Locate the red blood cells and classify each one as P. falciparum-infected, uninfected, or of indeterminate infection status.
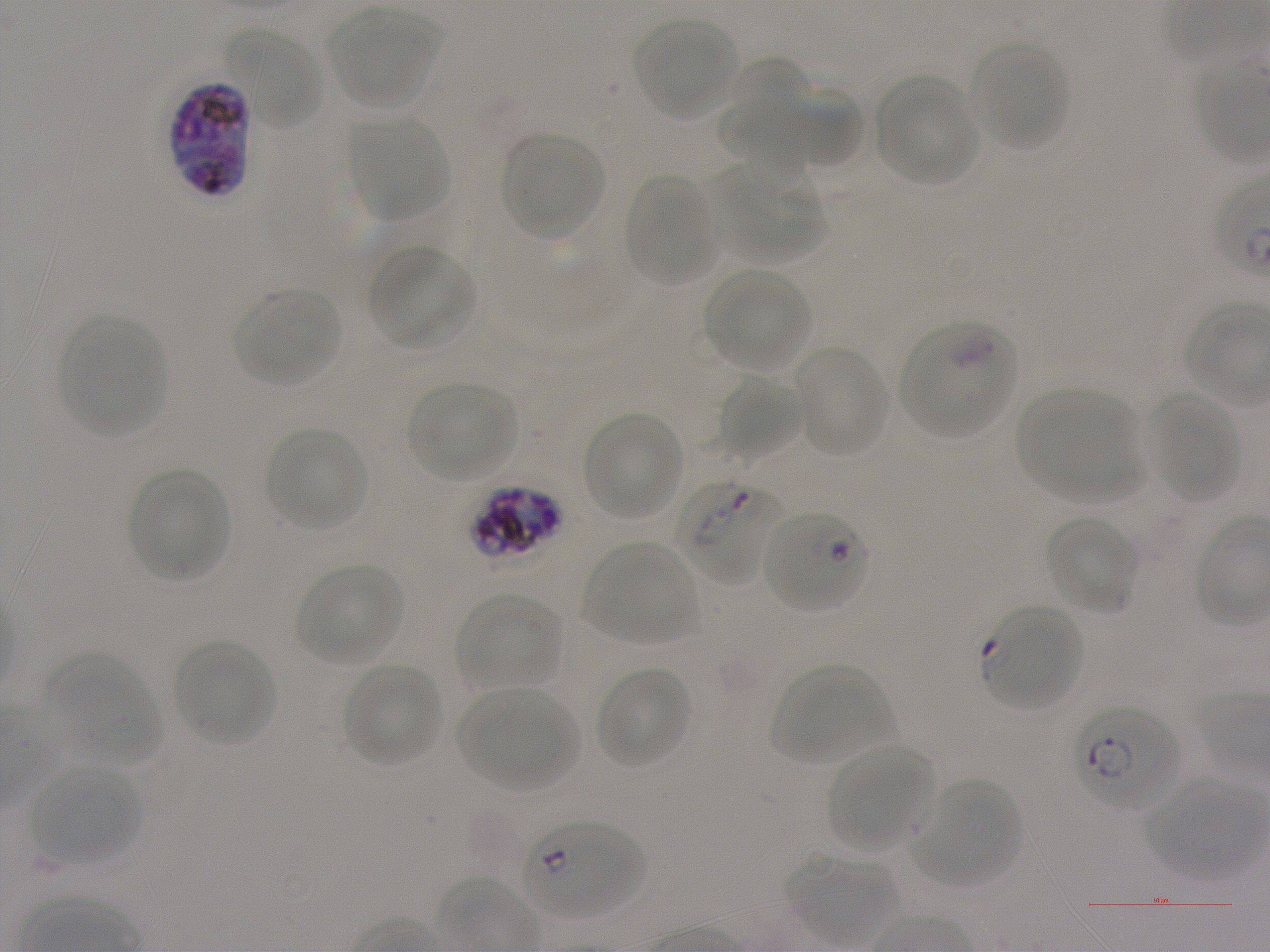

Approximate bounding boxes as (x1, y1, x2, y2) in pixels. Not every red blood cell is marked. A life-cycle stage — or a range of stages, where the recorded stages span more than one — follows each staged infected red blood cell.
Infected red blood cells: (169, 80, 252, 198); (674, 479, 785, 585) early ring to early trophozoite; (470, 484, 564, 561) schizont; (762, 508, 871, 613) early ring; (980, 604, 1083, 712) ring; (1072, 704, 1183, 812) early ring to early trophozoite; (522, 819, 647, 920) ring.
Red blood cells of indeterminate infection status: (898, 322, 1016, 437).
Uninfected red blood cells: (328, 9, 443, 111), (634, 18, 738, 120), (227, 25, 326, 130), (970, 42, 1070, 151), (725, 56, 812, 193), (873, 74, 979, 186), (783, 84, 864, 170), (716, 98, 813, 161), (347, 115, 450, 222), (502, 133, 605, 240), (712, 164, 824, 263), (624, 175, 718, 285), (367, 245, 477, 352), (703, 268, 812, 371), (234, 289, 341, 388), (60, 315, 167, 437), (792, 344, 890, 458), (716, 374, 803, 460), (406, 380, 519, 483), (1016, 389, 1139, 502), (1146, 391, 1240, 502), (583, 413, 684, 521), (265, 427, 369, 531), (127, 468, 232, 584), (1044, 516, 1139, 616), (582, 540, 699, 645), (295, 563, 405, 666), (455, 593, 562, 692), (174, 640, 276, 747), (41, 654, 161, 766), (342, 661, 442, 767), (770, 662, 893, 765), (595, 666, 693, 770), (457, 688, 581, 791), (826, 744, 937, 853), (29, 767, 143, 865), (1143, 779, 1268, 880), (912, 780, 1021, 888), (786, 855, 896, 946).

preparation = thin blood smear
life-cycle stages observed = ring, schizont
donor blood group = A+
culture = in-vitro P. falciparum strain NF54, static
field of view = one from this slide
stain = Giemsa
objective = 100x, oil immersion, numerical aperture 1.25
image size = 1270×952 pixels